Outline each uninfected red blood cell.
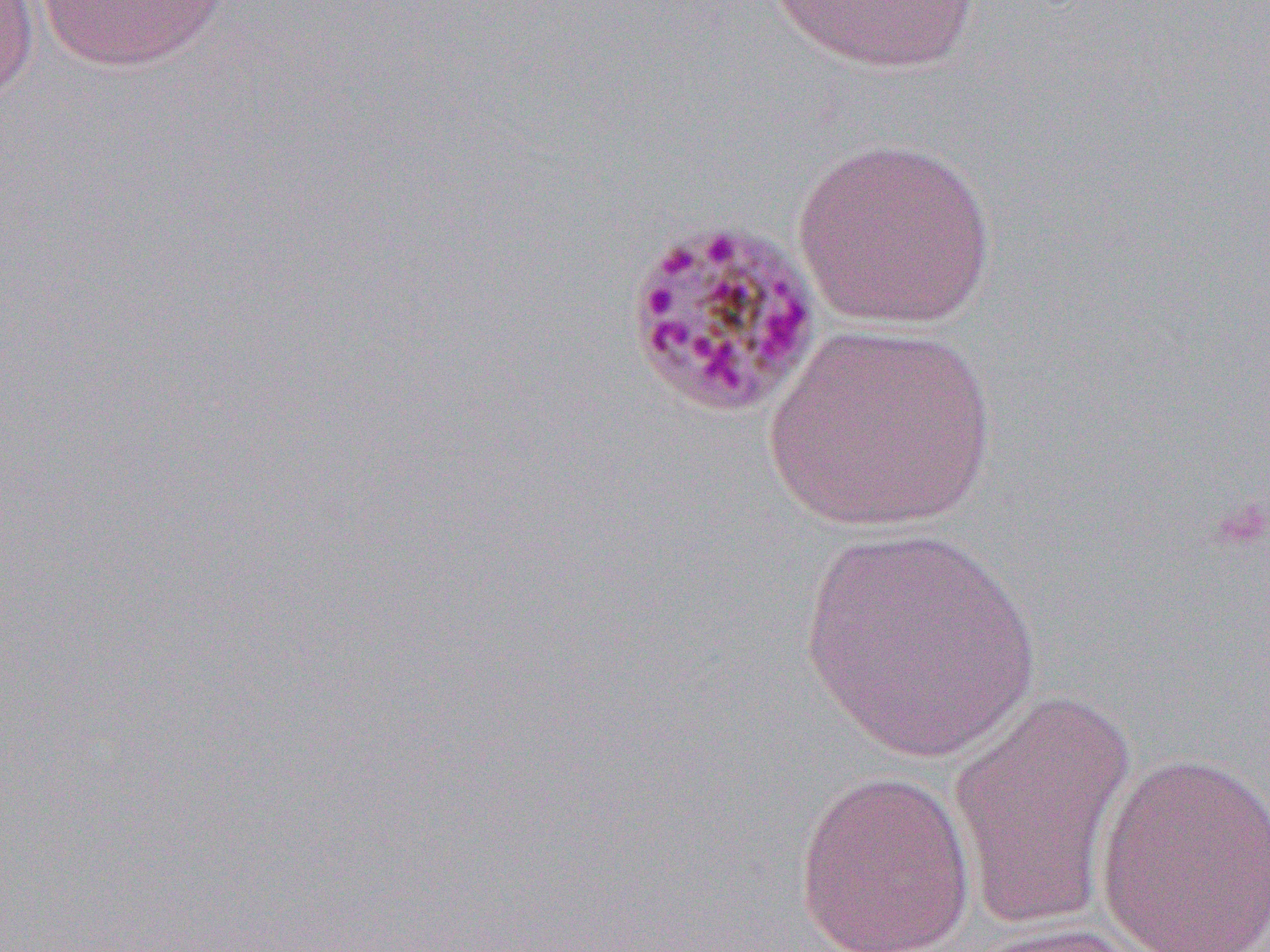
Approximate bounding boxes as [x1, y1, x2, y2] in pixels.
Uninfected red blood cells: [0, 0, 40, 107], [34, 0, 231, 72], [765, 0, 983, 74], [791, 135, 998, 330], [762, 323, 997, 534], [797, 525, 1041, 769], [946, 690, 1138, 929], [1094, 750, 1270, 950], [793, 769, 976, 952], [959, 919, 1165, 951].

Summary:
  - Slide-level diagnosis: Plasmodium malariae
  - Modality: optical microscopy
  - Image size: 1270×952 pixels
  - Field of view: one of a larger specimen
  - Preparation: thin blood film
  - Magnification: 1000x